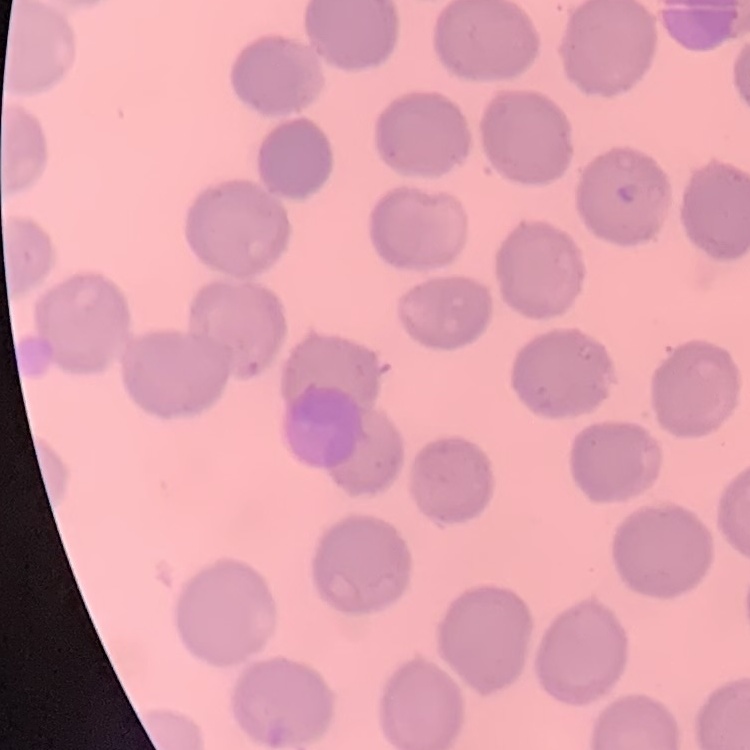 The red blood cells exhibit no rouleaux formation. Square crop of a larger photomicrograph. Stained with either Field's or Giemsa. Thin blood smear.